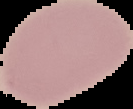
image type = cell region segmented out of the field of view; surrounding area masked to black
malaria status = uninfected
preparation = thin blood smear
image size = 133×109 pixels